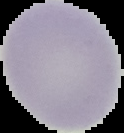 The area outside the segmented cell region is set to black. Image is 124×133 pixels. From a thin blood smear. Malaria status: uninfected.